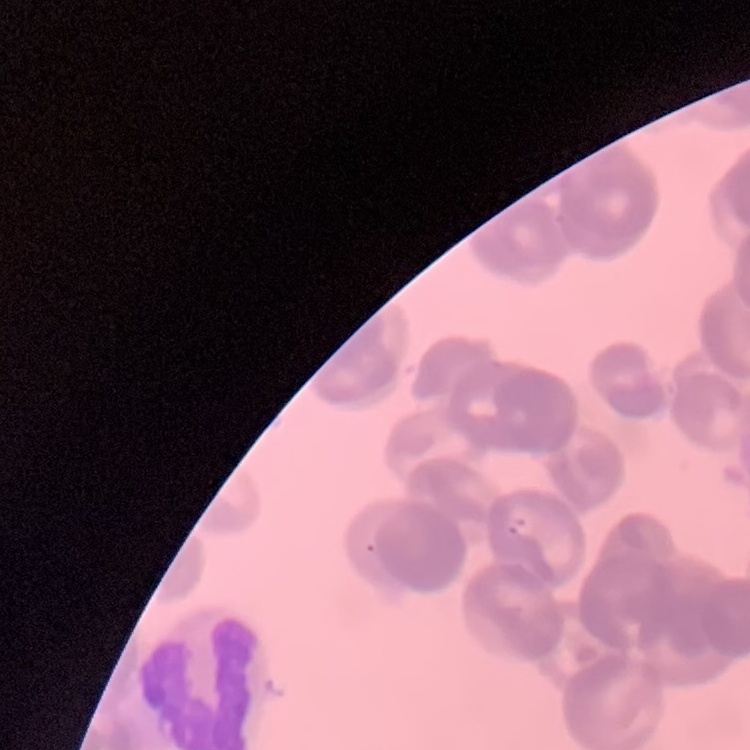
erythrocyte morphology = rouleaux formation
stain = Field's or Giemsa
preparation = thin peripheral smear
image type = square crop of a larger photomicrograph